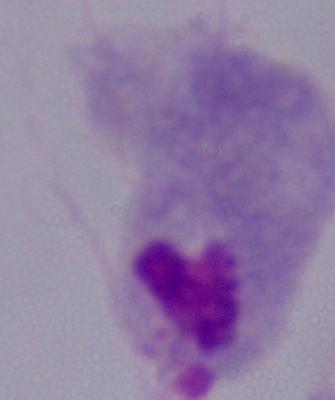

Summary:
  - Identification: trichomonad
  - Modality: micrograph
  - Magnification: 1000x